Classify this cell by malaria status.
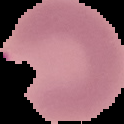
It is parasitized.

Image is 124×124 pixels. Segmented cell region on a black background. From a thin blood smear.